Outline each blood parasite and name the species.
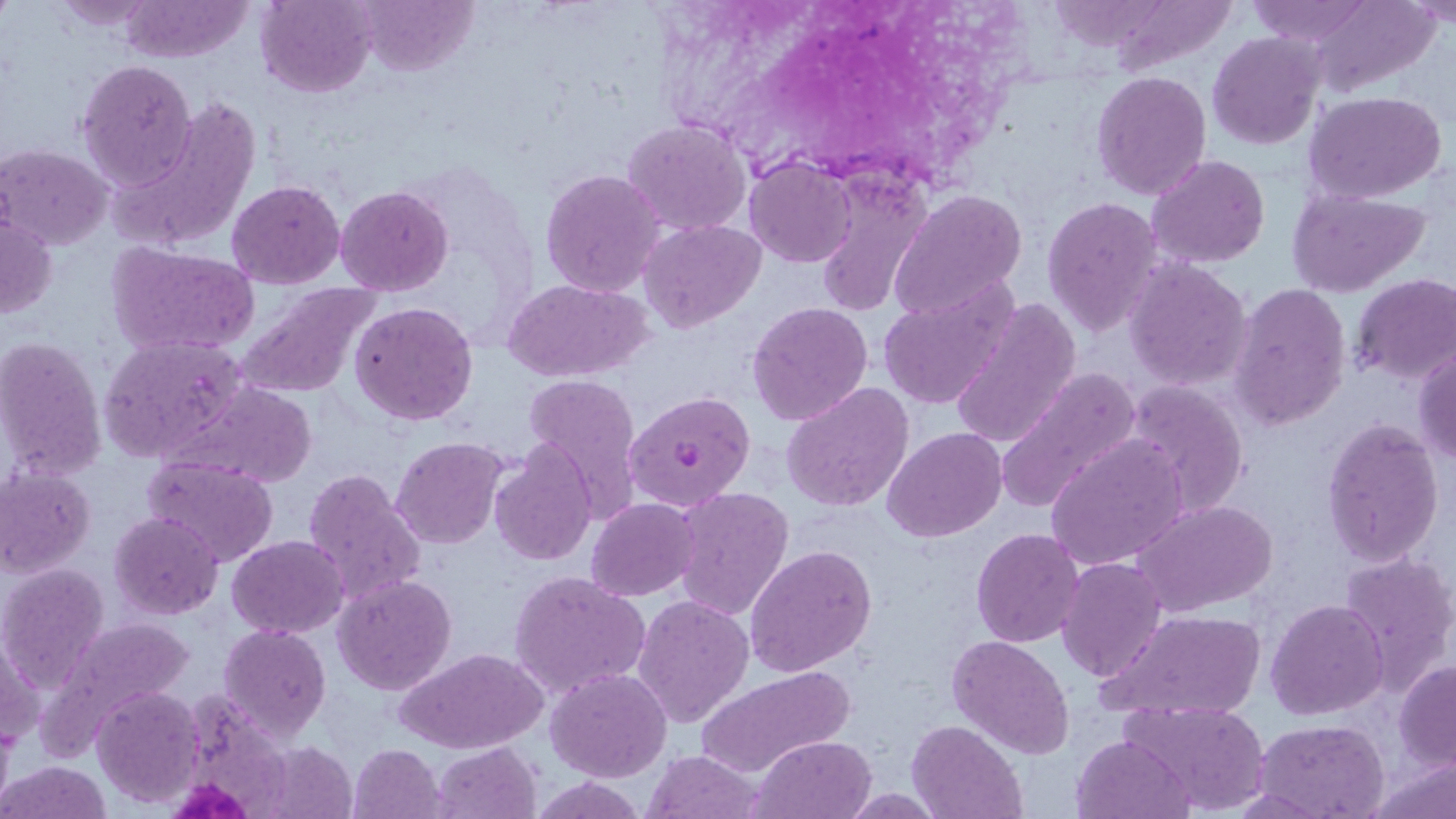

Approximate bounding boxes as [x1, y1, x2, y2] in pixels.
Plasmodium falciparum-infected red blood cells: [624, 391, 755, 511].
No Plasmodium ovale, Plasmodium malariae, Plasmodium vivax, Babesia divergens, or Trypanosoma brucei observed.

Uninfected red blood cell locations: [48, 0, 164, 29], [120, 0, 254, 61], [256, 0, 377, 98], [355, 0, 478, 74], [1245, 0, 1376, 47], [1309, 0, 1440, 98], [1209, 34, 1323, 148], [76, 59, 198, 189], [1092, 71, 1212, 201], [1305, 92, 1446, 204], [114, 98, 263, 250], [622, 119, 752, 237], [2, 143, 113, 250], [1147, 154, 1271, 270], [744, 157, 857, 268], [539, 169, 667, 298], [810, 169, 933, 318], [226, 179, 346, 289], [335, 184, 454, 297], [888, 189, 1027, 323], [1288, 189, 1430, 296], [1042, 197, 1164, 338], [0, 212, 57, 319], [638, 218, 766, 332], [107, 242, 261, 358], [1124, 259, 1253, 391], [1351, 275, 1456, 386], [503, 278, 651, 384], [876, 280, 1018, 411], [233, 282, 384, 398], [1231, 282, 1351, 431], [949, 299, 1084, 449], [350, 301, 477, 426], [746, 301, 874, 426], [97, 333, 252, 465], [0, 335, 107, 482], [1414, 349, 1456, 467], [993, 365, 1141, 515], [522, 377, 645, 526], [1123, 379, 1250, 518], [165, 380, 319, 487], [781, 382, 915, 514], [1320, 417, 1445, 567], [882, 426, 1007, 542], [1045, 436, 1189, 570], [391, 438, 509, 548], [490, 443, 595, 566], [142, 456, 280, 567], [0, 467, 97, 578], [302, 468, 427, 607], [671, 486, 794, 620], [587, 498, 699, 600], [1133, 498, 1280, 615], [110, 512, 224, 620], [971, 528, 1085, 647], [226, 536, 349, 638], [745, 543, 877, 677], [1340, 549, 1456, 691], [1058, 556, 1168, 682], [2, 564, 109, 689], [509, 570, 651, 702], [333, 574, 456, 695], [632, 593, 755, 728], [1265, 599, 1388, 720], [1094, 609, 1270, 724], [40, 616, 194, 750], [218, 624, 331, 740], [1, 633, 42, 749], [948, 633, 1075, 759], [395, 646, 546, 752], [1394, 661, 1456, 770], [695, 664, 852, 775], [547, 667, 673, 782], [190, 684, 286, 814], [93, 685, 206, 807], [1116, 700, 1270, 815], [908, 720, 1026, 819], [1256, 720, 1388, 817], [1071, 733, 1195, 819], [752, 734, 875, 818], [258, 741, 356, 818], [431, 742, 541, 818], [348, 744, 446, 819], [642, 750, 765, 819], [1369, 752, 1456, 819], [0, 760, 111, 819], [534, 777, 644, 818]. Platelet locations: [180, 779, 253, 819]. Slide-level diagnosis: Plasmodium falciparum. Captured at 1000x magnification. May-Grünwald-Giemsa-stained preparation. Optical microscopy. One field of a larger specimen. Thin blood smear. Image is 1456×819 pixels.